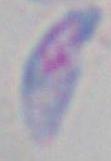 1000x magnification. Photomicrograph. Toxoplasma gondii is seen.